Locate and identify every blood parasite.
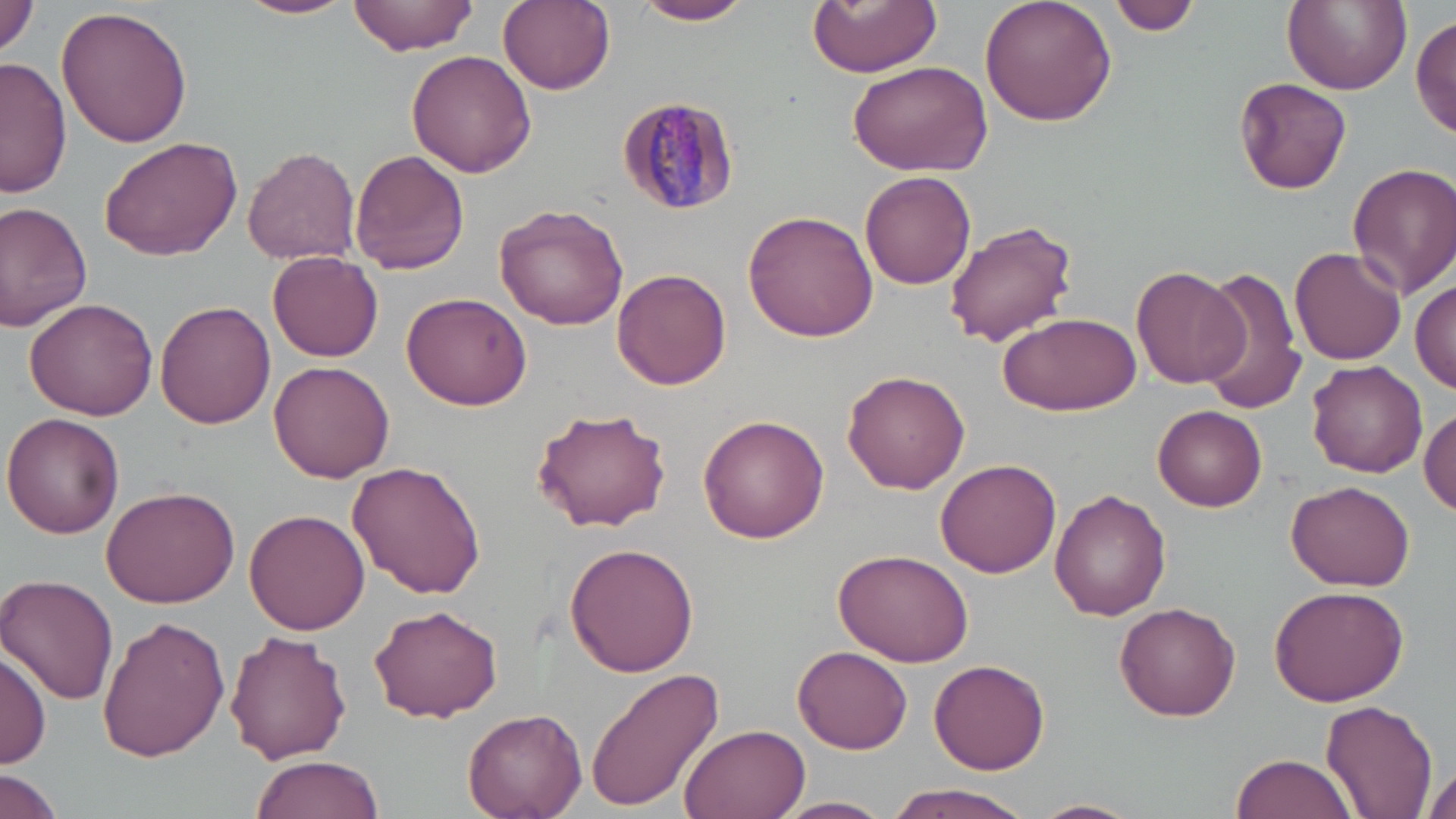
Approximate bounding boxes as (x1, y1, x2, y2) in pixels.
Plasmodium malariae-infected red blood cells: (615, 93, 741, 216).
No Plasmodium falciparum, Plasmodium ovale, Plasmodium vivax, Babesia divergens, or Trypanosoma brucei observed.

Summary:
  - Uninfected red blood cell locations: (0, 0, 39, 57), (236, 0, 356, 20), (348, 0, 479, 55), (498, 0, 615, 94), (633, 0, 757, 25), (807, 0, 942, 76), (979, 0, 1118, 127), (1109, 0, 1200, 37), (1284, 0, 1409, 95), (54, 4, 194, 149), (1412, 13, 1456, 140), (405, 50, 534, 178), (845, 56, 994, 177), (1, 58, 73, 200), (1235, 77, 1352, 194), (101, 134, 244, 261), (243, 145, 361, 264), (349, 151, 470, 277), (1347, 162, 1456, 298), (860, 171, 976, 291), (869, 179, 1064, 314), (0, 202, 94, 332), (493, 202, 629, 329), (743, 210, 878, 342), (943, 219, 1078, 346), (1289, 247, 1408, 366), (268, 251, 384, 362), (1132, 266, 1247, 389), (1196, 266, 1307, 414), (612, 268, 730, 391), (1411, 279, 1456, 393), (400, 290, 534, 410), (25, 297, 158, 422), (154, 300, 274, 428), (998, 309, 1142, 417), (269, 360, 396, 483), (1307, 360, 1428, 476), (842, 370, 970, 494), (1153, 405, 1266, 509), (532, 407, 672, 533), (1419, 407, 1455, 515), (2, 412, 125, 537), (697, 414, 829, 544), (935, 459, 1061, 578), (345, 462, 487, 598), (1286, 479, 1415, 591), (101, 484, 241, 608), (1049, 489, 1170, 622), (244, 510, 370, 635), (564, 544, 698, 676), (831, 545, 973, 666), (3, 575, 120, 706), (1267, 584, 1408, 707), (1113, 601, 1241, 720), (367, 605, 506, 723), (97, 616, 227, 761), (225, 631, 352, 764), (793, 647, 912, 754), (0, 648, 50, 771), (929, 655, 1051, 775), (587, 667, 725, 811), (1321, 699, 1438, 818), (461, 708, 585, 819), (680, 723, 811, 819), (1233, 752, 1359, 819), (248, 754, 385, 819), (1419, 760, 1453, 819), (0, 769, 65, 819), (879, 783, 1036, 819), (776, 796, 893, 819), (1027, 798, 1142, 819)
  - Slide-level diagnosis: Plasmodium malariae
  - Stain: May-Grünwald-Giemsa
  - Preparation: thin blood smear
  - Image size: 1456×819 pixels
  - Field of view: single
  - Magnification: 1000x
  - Modality: optical microscopy